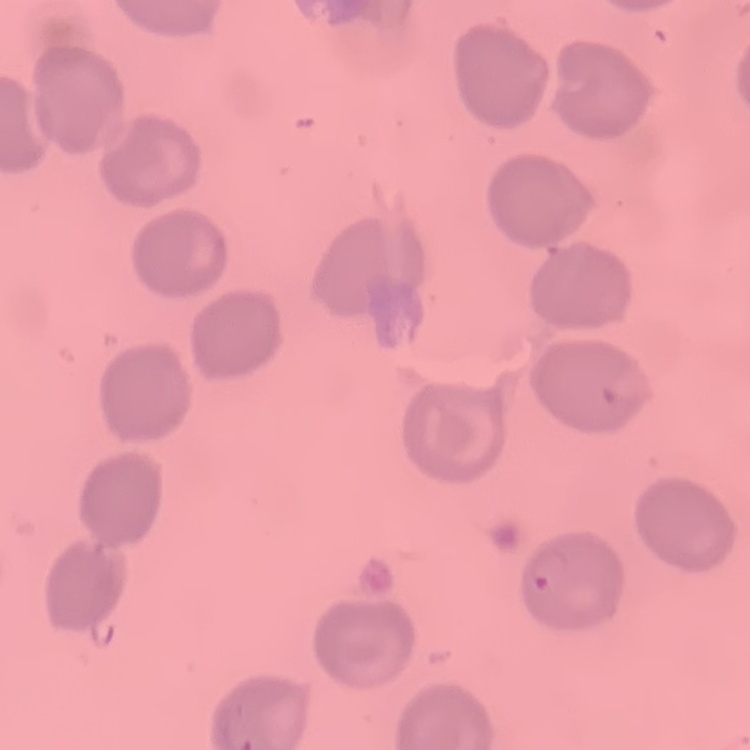

Summary:
  - Red blood cell morphology: no rouleaux formation
  - Stain: Field's or Giemsa
  - Preparation: thin blood smear
  - Image type: square crop of a larger photomicrograph